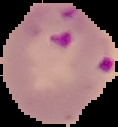

Summary:
  - Image size: 118×127 pixels
  - Preparation: thin blood film
  - Result: malaria parasites identified
  - Image type: segmented cell region with the area outside set to black